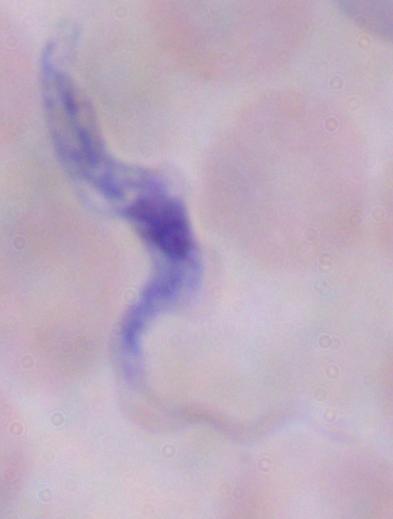

Summary:
  - Magnification: 1000x
  - Identification: trypanosome
  - Modality: photomicrograph